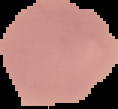

Summary:
  - Preparation: thin blood smear
  - Result: no Plasmodium parasites seen
  - Image type: segmented cell region on a black background
  - Image size: 118×109 pixels